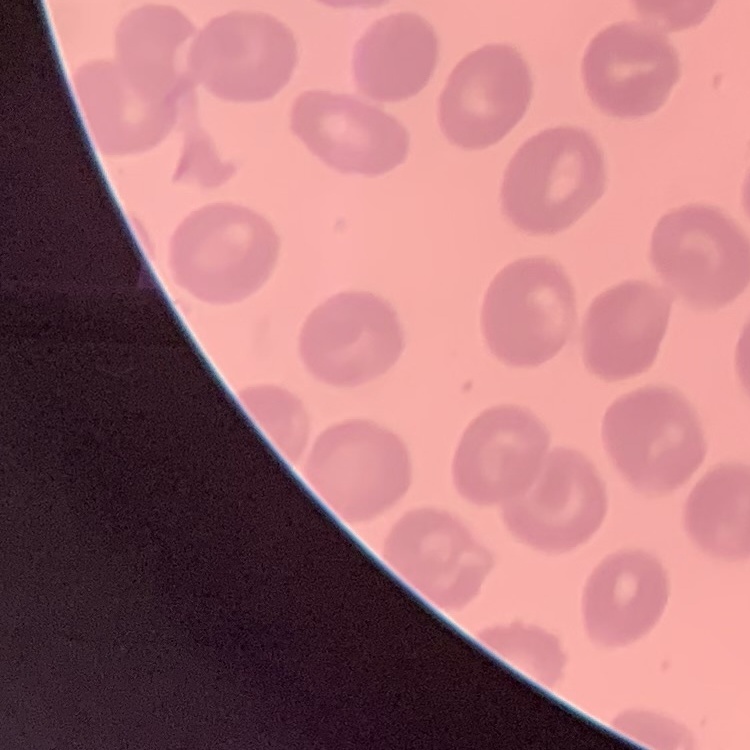
red blood cell morphology = no rouleaux formation
image type = one tile cut from a larger photomicrograph
preparation = thin blood film
stain = Field's or Giemsa